Name the parasite shown.
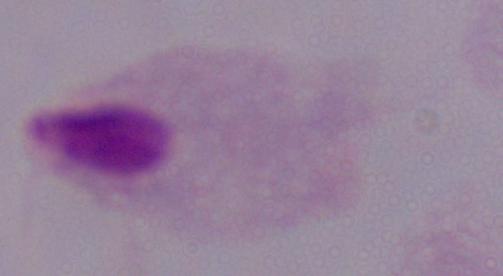

A trichomonad.

Summary:
  - Magnification: 1000x
  - Modality: micrograph